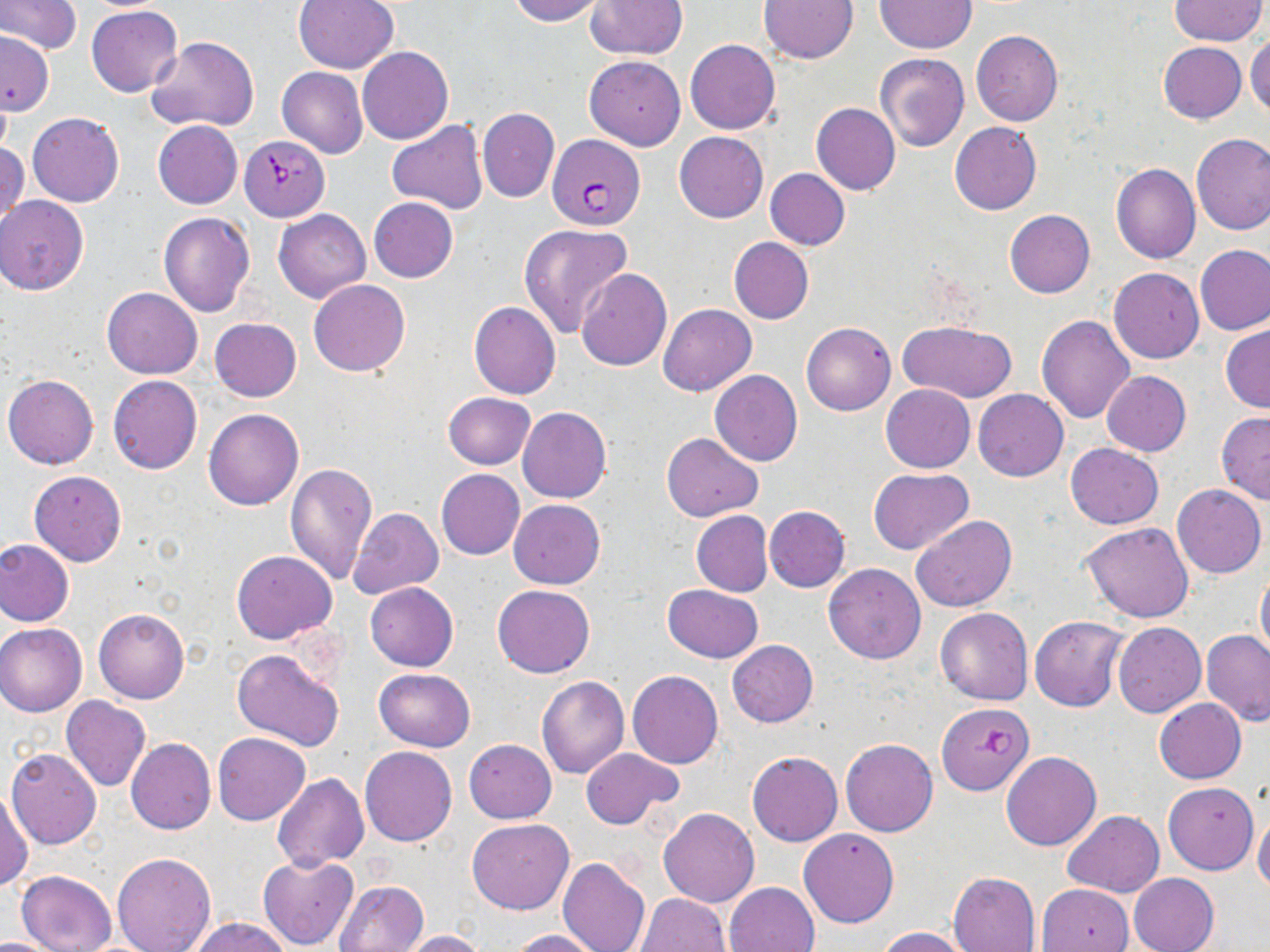
{
  "slide_level_diagnosis": "Plasmodium falciparum",
  "magnification": "1000x",
  "plasmodium_falciparum_infected_red_blood_cell_locations": "approximate bounding boxes as (x1, y1, x2, y2) in pixels: (548, 134, 646, 230), (238, 136, 329, 221), (937, 701, 1033, 795)",
  "field_of_view": "one of a larger specimen",
  "uninfected_red_blood_cell_locations": "approximate bounding boxes as (x1, y1, x2, y2) in pixels: (1, 0, 81, 54), (507, 0, 609, 25), (759, 0, 860, 64), (1171, 0, 1266, 46), (292, 1, 399, 73), (586, 1, 687, 59), (874, 1, 976, 52), (87, 6, 183, 97), (970, 29, 1063, 126), (0, 33, 56, 112), (1246, 33, 1270, 120), (147, 37, 257, 132), (685, 40, 781, 134), (1158, 42, 1247, 123), (357, 46, 454, 145), (876, 53, 969, 152), (584, 55, 686, 150), (277, 67, 368, 159), (811, 103, 900, 195), (477, 108, 560, 202), (28, 112, 124, 207), (387, 119, 489, 215), (152, 120, 242, 209), (950, 122, 1041, 215), (674, 131, 768, 223), (1191, 133, 1270, 235), (0, 138, 28, 230), (1110, 164, 1200, 263), (764, 169, 849, 250), (0, 196, 90, 295), (368, 197, 457, 282), (273, 209, 370, 303), (1005, 209, 1095, 297), (158, 212, 256, 317), (518, 223, 632, 338), (729, 237, 814, 324), (1195, 245, 1270, 335), (576, 268, 671, 373), (1109, 268, 1204, 363), (307, 279, 411, 377), (102, 287, 203, 379), (469, 301, 560, 400), (659, 303, 756, 396), (1036, 316, 1134, 423), (210, 317, 301, 401), (899, 321, 1019, 401), (802, 322, 896, 415), (1221, 324, 1270, 413), (710, 370, 804, 466), (1101, 371, 1190, 457), (3, 374, 99, 469), (107, 375, 202, 474), (880, 384, 975, 473), (974, 389, 1068, 481), (443, 392, 536, 470), (518, 407, 611, 502), (204, 408, 304, 511), (1216, 412, 1270, 504), (662, 431, 763, 521), (1065, 444, 1163, 529), (284, 463, 377, 586), (867, 467, 975, 554), (436, 468, 524, 559), (29, 470, 126, 566), (1172, 484, 1266, 578), (509, 499, 605, 588), (763, 506, 850, 592), (349, 507, 443, 599), (691, 510, 772, 596), (911, 514, 1015, 612), (1081, 523, 1194, 624), (0, 539, 75, 626), (231, 550, 336, 645), (823, 563, 927, 664), (1256, 569, 1270, 663), (365, 583, 458, 671), (493, 584, 594, 677), (662, 585, 764, 662), (94, 608, 189, 704), (935, 608, 1032, 705), (1029, 616, 1127, 711), (1113, 622, 1206, 717), (0, 623, 88, 717), (1203, 629, 1270, 725), (727, 639, 818, 726), (232, 648, 345, 751), (374, 669, 475, 751), (627, 670, 722, 768), (537, 675, 629, 778), (61, 696, 151, 791), (1155, 698, 1246, 783), (213, 732, 310, 825), (126, 738, 215, 834), (464, 739, 556, 823), (840, 739, 937, 837), (360, 746, 458, 847), (579, 747, 683, 830), (7, 748, 101, 849), (748, 751, 842, 846), (1001, 751, 1101, 851), (274, 773, 369, 868), (1163, 781, 1258, 875), (1, 788, 32, 891), (658, 807, 760, 907), (1253, 809, 1270, 898), (1063, 810, 1164, 897), (466, 818, 574, 915), (799, 827, 899, 928), (111, 852, 216, 952), (258, 854, 359, 949), (557, 857, 650, 952), (17, 870, 117, 952), (949, 871, 1041, 952), (1129, 873, 1219, 952), (334, 879, 428, 952), (724, 882, 820, 952), (1036, 884, 1132, 952), (637, 893, 731, 952), (190, 916, 293, 952), (877, 927, 972, 952), (511, 929, 604, 952), (395, 930, 487, 951), (0, 934, 61, 951)",
  "image_size": "1270×952 pixels",
  "stain": "May-Grünwald-Giemsa",
  "preparation": "thin blood film",
  "modality": "light microscopy"
}